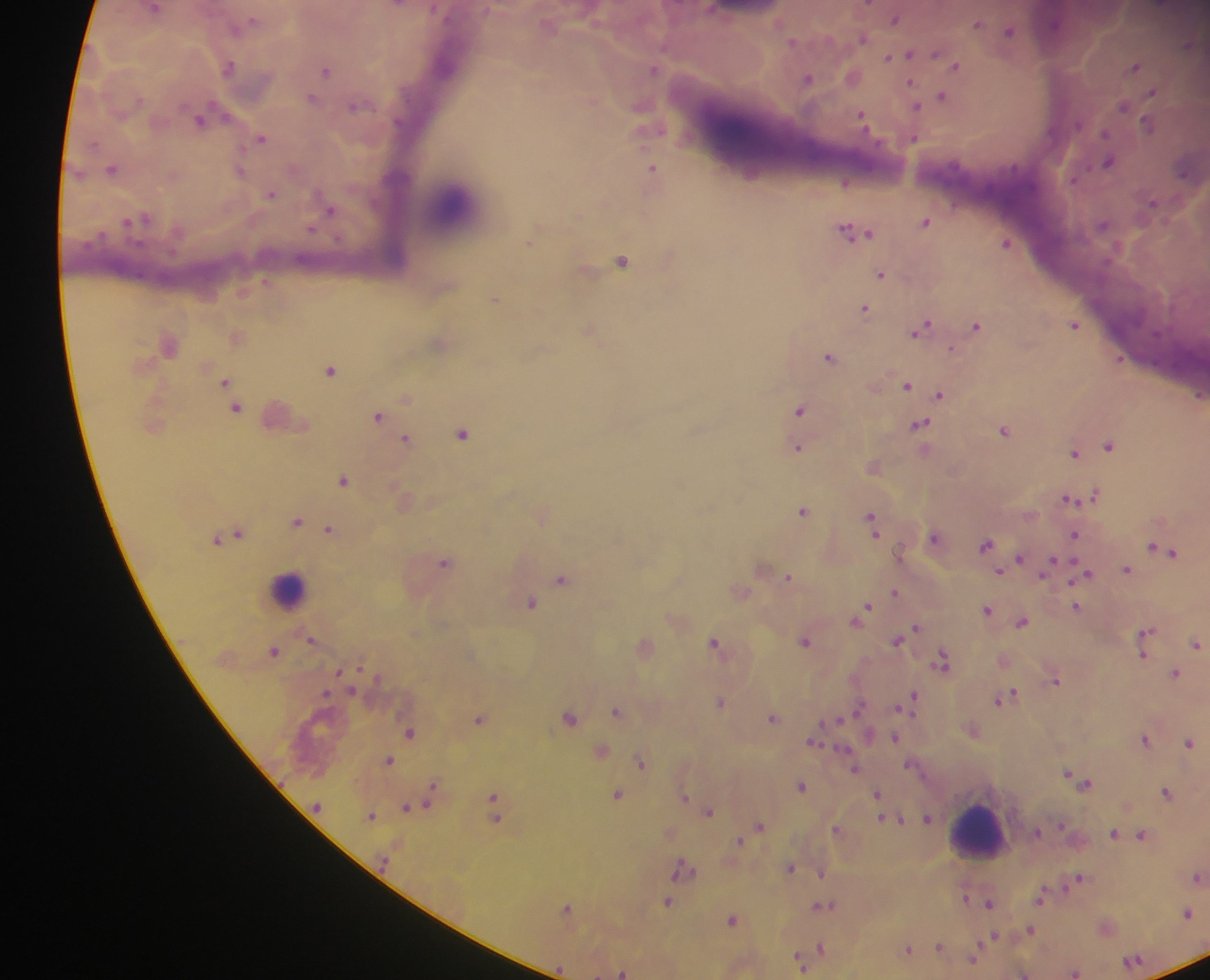

Approximate centers as {x, y} in pixels.
Summary:
  - Malaria parasite locations: {868, 4}, {895, 19}, {978, 24}, {1010, 32}, {862, 38}, {793, 41}, {1188, 46}, {909, 54}, {935, 54}, {889, 57}, {230, 67}, {956, 67}, {1135, 68}, {653, 69}, {326, 70}, {807, 79}, {911, 85}, {1151, 93}, {942, 96}, {312, 97}, {356, 106}, {1125, 106}, {915, 107}, {861, 118}, {200, 122}, {1148, 124}, {1105, 133}, {262, 138}, {913, 138}, {1109, 162}, {112, 169}, {653, 169}, {240, 172}, {1075, 179}, {846, 183}, {271, 194}, {1153, 204}, {329, 211}, {145, 219}, {926, 221}, {129, 222}, {855, 231}, {529, 241}, {1005, 243}, {622, 261}, {882, 274}, {495, 299}, {864, 308}, {1074, 325}, {976, 326}, {922, 327}, {951, 349}, {829, 357}, {1120, 360}, {330, 370}, {225, 382}, {907, 386}, {941, 394}, {1200, 395}, {235, 408}, {800, 411}, {377, 416}, {919, 426}, {1004, 430}, {463, 434}, {406, 439}, {1109, 445}, {797, 448}, {1074, 452}, {343, 480}, {1095, 494}, {1069, 498}, {803, 510}, {297, 522}, {872, 522}, {329, 529}, {238, 532}, {1075, 535}, {934, 537}, {985, 544}, {1159, 548}, {1168, 553}, {1019, 559}, {444, 562}, {1049, 565}, {1127, 570}, {1087, 574}, {789, 577}, {561, 578}, {895, 592}, {531, 603}, {1076, 608}, {864, 610}, {987, 610}, {859, 617}, {1022, 622}, {914, 629}, {1145, 634}, {310, 639}, {898, 639}, {715, 641}, {805, 641}, {1144, 644}, {1196, 645}, {274, 651}, {1143, 655}, {943, 661}, {1176, 674}, {1057, 681}, {1005, 698}, {910, 700}, {720, 702}, {858, 708}, {617, 712}, {570, 717}, {772, 718}, {479, 719}, {835, 720}, {410, 733}, {895, 738}, {1145, 738}, {814, 740}, {1188, 743}, {389, 761}, {642, 763}, {910, 766}, {854, 768}, {1068, 772}, {1077, 779}, {1088, 783}, {801, 786}, {433, 787}, {1166, 792}, {617, 794}, {431, 795}, {877, 795}, {684, 798}, {407, 808}, {495, 808}, {709, 811}, {371, 815}, {928, 818}, {895, 820}, {760, 826}, {837, 829}, {1036, 831}, {1113, 834}, {1142, 835}, {739, 840}, {682, 867}, {790, 867}, {822, 873}, {1197, 877}, {1077, 879}, {1040, 896}, {667, 902}, {990, 903}, {822, 906}, {567, 908}, {1187, 913}, {733, 919}, {1031, 929}, {992, 937}, {939, 946}, {821, 948}, {908, 948}, {973, 957}, {799, 960}, {1132, 962}, {622, 972}, {1075, 972}
  - Leukocyte locations: {289, 588}, {978, 830}
  - Preparation: thick blood smear
  - Image size: 1210×980 pixels
  - Country: Ghana
  - Capture: mobile-phone photograph through a microscope
  - Field of view: single